Assess this cell for malaria.
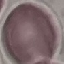

Uninfected.

Thin blood smear. Giemsa-stained preparation. Cell patch, automatically extracted from a larger field of view and resized to 64 × 64 pixels. Photographed with a smartphone camera at the microscope eyepiece.